Point out each leukocyte.
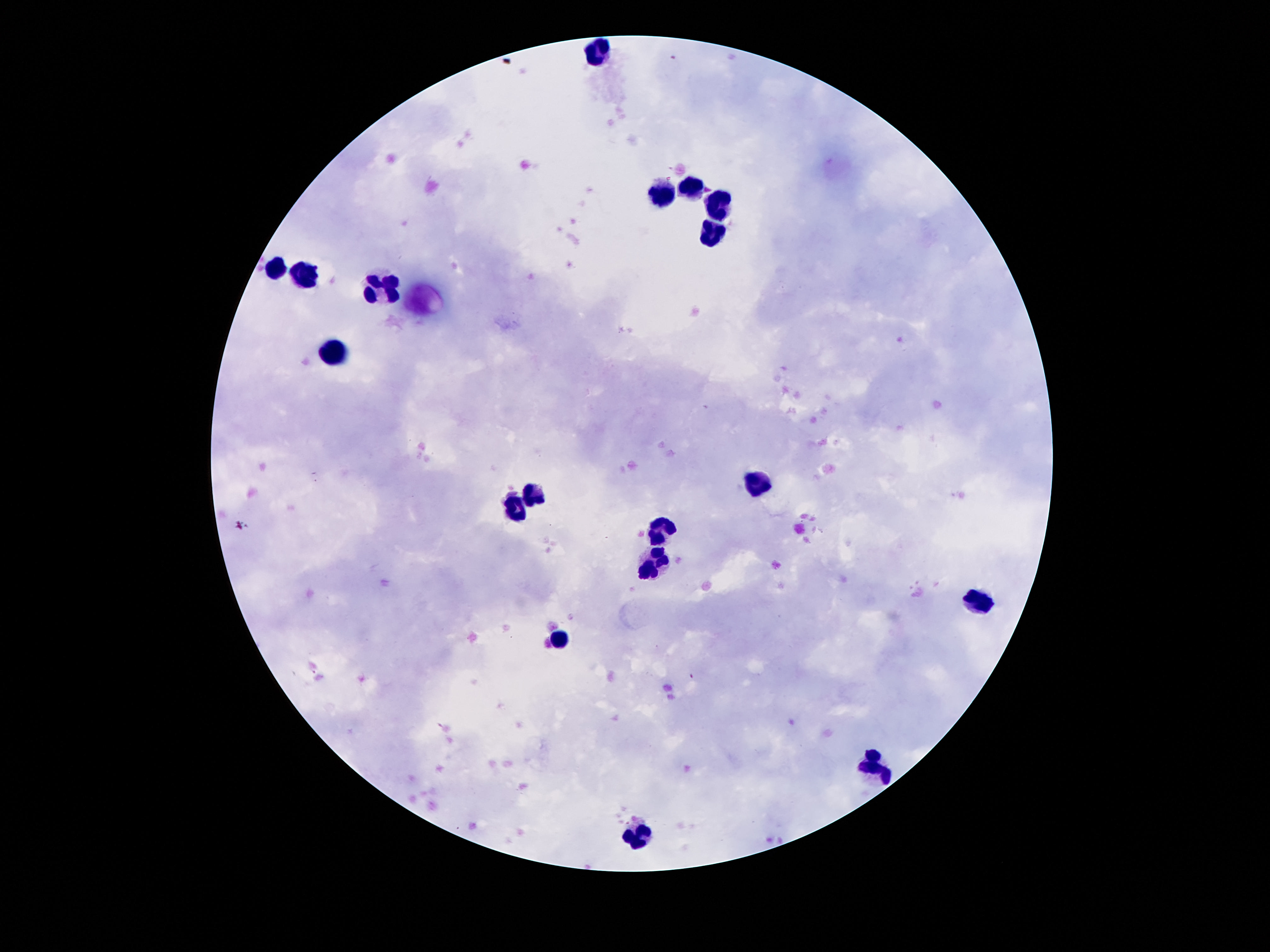

Approximate object centers, in pixels from the top-left corner.
Leukocytes: (x=598, y=53), (x=692, y=188), (x=663, y=194), (x=718, y=205), (x=712, y=232), (x=275, y=268), (x=306, y=278), (x=387, y=286), (x=337, y=352), (x=755, y=484), (x=533, y=492), (x=514, y=511), (x=661, y=533), (x=655, y=568), (x=983, y=601), (x=558, y=641), (x=872, y=765), (x=641, y=834).

Smartphone photograph taken through the microscope eyepiece. 100x magnification. Giemsa-stained preparation. One field from this slide. Image is 1270×952 pixels. Thick blood film. Patient malaria status: negative.